Comment on the morphology of the erythrocytes.
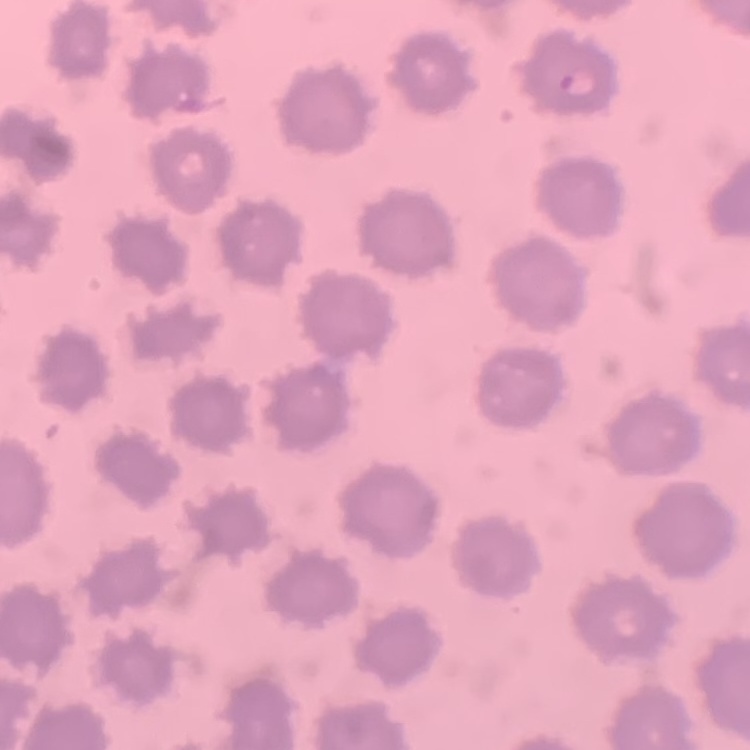

They show no rouleaux formation.

stain = Field's or Giemsa
image type = one tile cut from a larger photomicrograph
preparation = thin blood smear